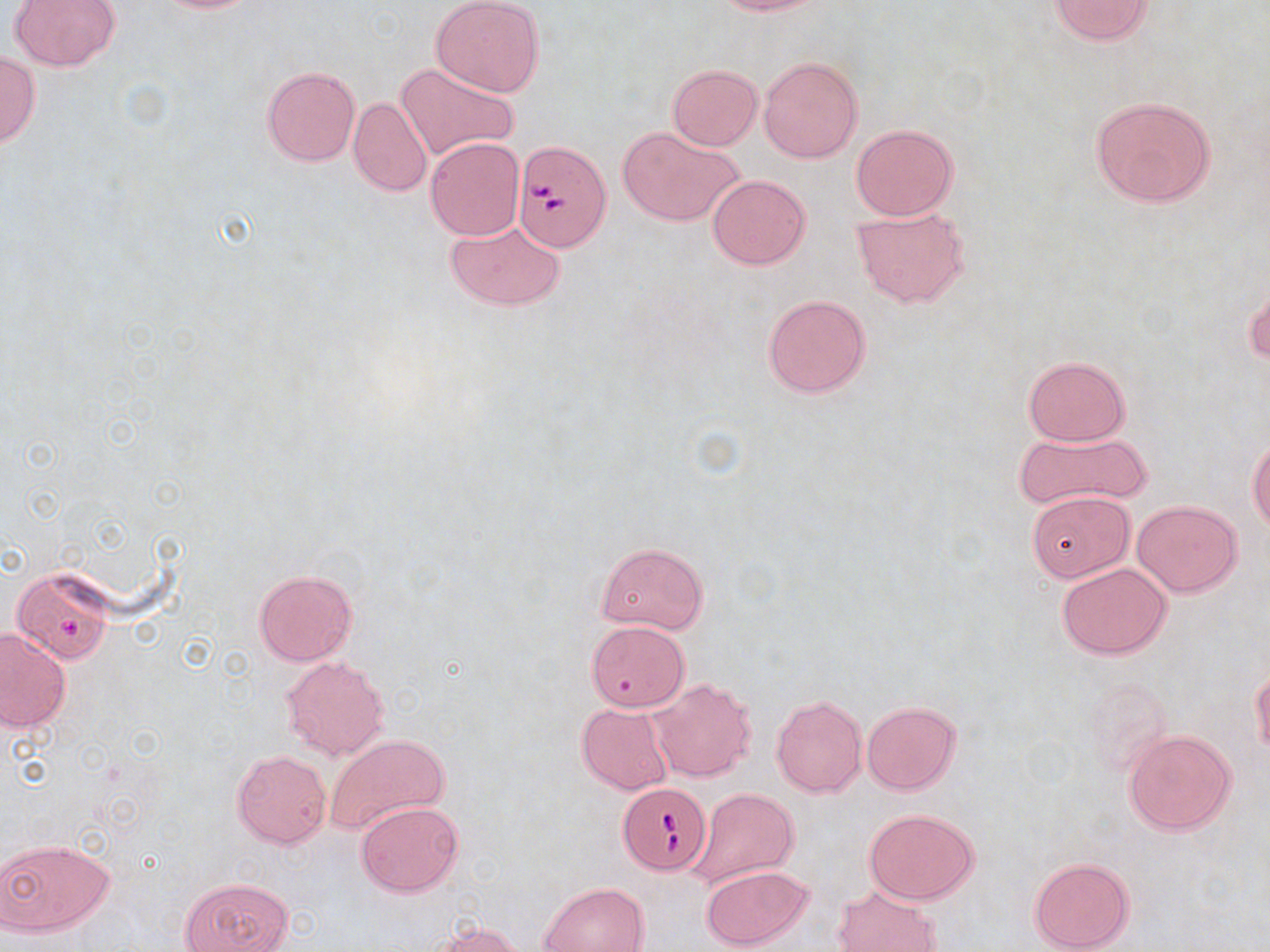 Approximate bounding boxes as (x1, y1, x2, y2) in pixels. Babesia divergens-infected red blood cell locations: (512, 140, 609, 251), (619, 784, 712, 875). Uninfected red blood cell locations: (145, 0, 261, 13), (431, 0, 545, 98), (710, 0, 828, 16), (1046, 0, 1155, 44), (10, 1, 120, 70), (0, 53, 39, 147), (759, 56, 863, 163), (396, 62, 518, 163), (667, 64, 762, 150), (262, 66, 360, 165), (1087, 95, 1216, 208), (348, 97, 431, 197), (851, 123, 958, 220), (618, 126, 745, 228), (425, 136, 525, 240), (707, 174, 811, 268), (851, 206, 971, 308), (444, 217, 566, 312), (1245, 282, 1268, 368), (762, 294, 871, 398), (1022, 355, 1128, 446), (1014, 431, 1150, 510), (1247, 435, 1269, 532), (1028, 490, 1135, 582), (1133, 499, 1241, 597), (598, 542, 709, 633), (1056, 561, 1173, 660), (252, 568, 358, 666), (16, 572, 113, 666), (587, 620, 690, 711), (1, 628, 69, 733), (281, 655, 390, 762), (1251, 667, 1270, 758), (647, 677, 756, 783), (1085, 678, 1174, 775), (771, 694, 866, 798), (862, 700, 960, 795), (577, 703, 674, 795), (1122, 729, 1238, 836), (325, 733, 449, 836), (232, 749, 331, 848), (688, 787, 800, 885), (356, 801, 462, 897), (864, 808, 979, 905), (0, 837, 113, 934), (1029, 857, 1135, 952), (700, 864, 813, 950), (181, 877, 292, 952), (541, 882, 649, 951), (833, 885, 940, 952), (429, 920, 527, 951). Slide-level diagnosis: Babesia divergens. Image is 1270×952 pixels. Thin blood film. Light microscopy. May-Grünwald-Giemsa stain. Single field of view. 1000x magnification.